Locate and identify every blood parasite.
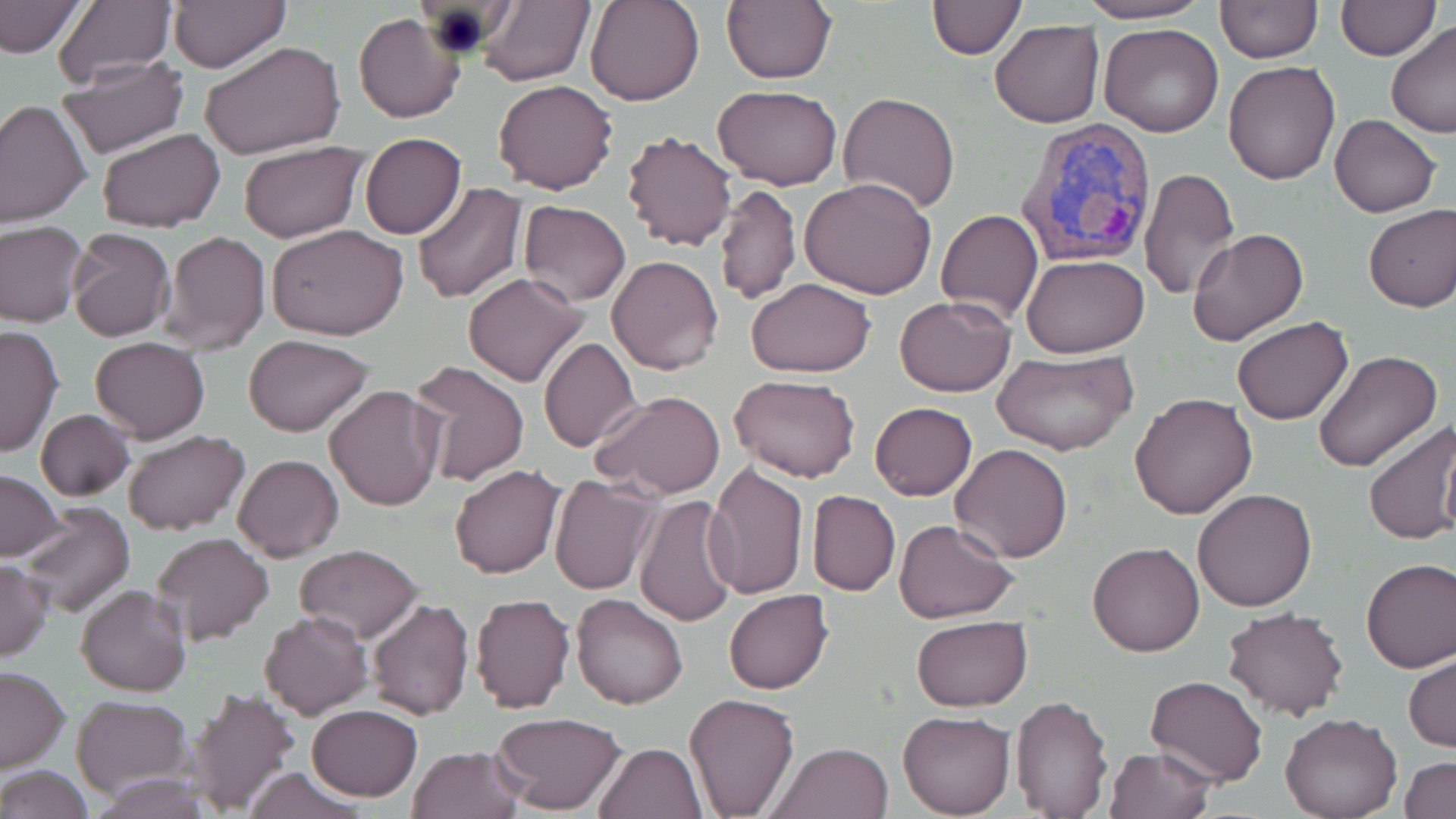
Approximate bounding boxes as [x1, y1, x2, y2] in pixels.
Plasmodium vivax-infected red blood cells: [1010, 120, 1159, 269].
No Plasmodium falciparum, Plasmodium ovale, Plasmodium malariae, Babesia divergens, or Trypanosoma brucei observed.

slide-level diagnosis = Plasmodium vivax
field of view = single
modality = optical microscopy
stain = May-Grünwald-Giemsa
image size = 1456×819 pixels
magnification = 1000x
uninfected red blood cell locations = approximate bounding boxes as [x1, y1, x2, y2] in pixels: [477, 0, 595, 87], [584, 0, 705, 106], [1073, 0, 1213, 24], [1336, 0, 1438, 59], [0, 1, 86, 61], [51, 1, 176, 90], [167, 1, 290, 72], [926, 1, 1025, 59], [1214, 1, 1322, 62], [721, 2, 836, 84], [354, 13, 465, 123], [991, 18, 1103, 127], [1385, 21, 1456, 139], [1098, 23, 1224, 137], [199, 40, 347, 161], [55, 55, 188, 159], [1224, 62, 1341, 185], [493, 79, 618, 195], [713, 85, 841, 191], [838, 92, 960, 214], [0, 100, 92, 228], [1331, 114, 1440, 218], [96, 127, 224, 234], [622, 130, 737, 251], [359, 133, 466, 239], [237, 142, 367, 242], [1139, 168, 1239, 300], [799, 178, 937, 299], [413, 181, 527, 304], [714, 183, 800, 303], [518, 200, 631, 305], [1363, 204, 1456, 312], [936, 209, 1043, 325], [0, 220, 88, 327], [266, 223, 408, 340], [65, 228, 176, 342], [158, 229, 270, 356], [1187, 229, 1307, 346], [1021, 252, 1150, 357], [606, 254, 723, 374], [463, 273, 588, 388], [746, 277, 876, 378], [894, 295, 1017, 397], [1232, 318, 1355, 426], [0, 323, 64, 458], [245, 334, 374, 437], [89, 337, 210, 443], [539, 338, 640, 453], [992, 350, 1137, 459], [1312, 351, 1441, 473], [407, 360, 531, 487], [728, 374, 860, 483], [324, 384, 445, 511], [590, 390, 726, 499], [1128, 392, 1260, 520], [870, 402, 977, 501], [35, 408, 136, 502], [1362, 419, 1456, 547], [121, 429, 250, 536], [950, 443, 1074, 563], [232, 452, 344, 561], [705, 462, 810, 600], [449, 463, 566, 580], [0, 471, 63, 560], [548, 473, 660, 597], [1191, 488, 1318, 611], [807, 489, 899, 596], [633, 494, 741, 628], [15, 501, 136, 618], [893, 519, 1018, 621], [147, 532, 274, 646], [1087, 541, 1206, 657], [293, 544, 424, 641], [1360, 557, 1456, 673], [0, 560, 52, 662], [76, 585, 192, 697], [723, 590, 834, 694], [470, 593, 575, 714], [571, 593, 688, 710], [367, 597, 475, 720], [1220, 607, 1348, 720], [259, 610, 372, 719], [911, 616, 1031, 710], [1405, 653, 1455, 752], [0, 667, 70, 773], [1145, 675, 1270, 788], [183, 686, 300, 817], [683, 692, 800, 817], [1009, 693, 1112, 816], [72, 695, 193, 801], [308, 704, 421, 800], [897, 709, 1014, 818], [491, 712, 625, 814], [1280, 713, 1401, 818], [595, 742, 706, 819], [768, 742, 895, 819], [406, 746, 525, 819], [1103, 747, 1216, 819], [1401, 756, 1456, 818], [0, 765, 94, 819], [241, 766, 369, 819], [91, 771, 215, 818]
preparation = thin blood smear